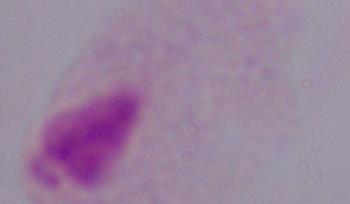
magnification = 1000x
identification = trichomonad
modality = micrograph